Give the extent of all Plasmodium malariae-infected red blood cells.
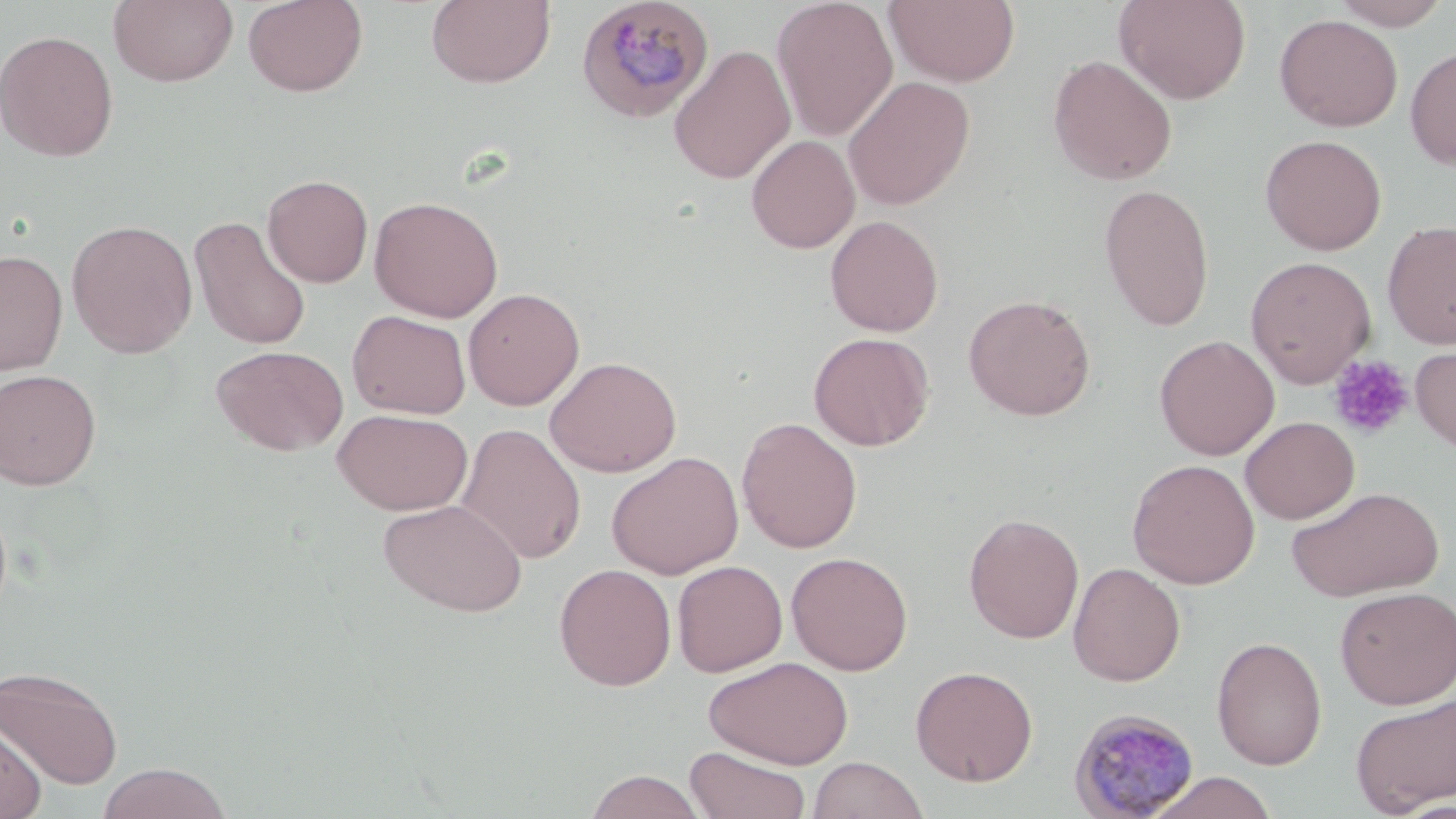

Approximate bounding boxes as named x1/y1/x2/y2 corners in pixels.
Plasmodium malariae-infected red blood cells: (x1=575, y1=0, x2=715, y2=123), (x1=1067, y1=708, x2=1201, y2=819).

Summary:
  - Platelet locations: (x1=1327, y1=354, x2=1414, y2=439)
  - Uninfected red blood cell locations: (x1=108, y1=0, x2=239, y2=87), (x1=242, y1=0, x2=368, y2=97), (x1=426, y1=0, x2=556, y2=89), (x1=772, y1=0, x2=898, y2=141), (x1=884, y1=0, x2=1021, y2=87), (x1=1114, y1=0, x2=1251, y2=104), (x1=1327, y1=0, x2=1451, y2=29), (x1=1274, y1=14, x2=1403, y2=132), (x1=0, y1=29, x2=119, y2=162), (x1=668, y1=44, x2=795, y2=184), (x1=1405, y1=45, x2=1456, y2=171), (x1=1047, y1=54, x2=1178, y2=186), (x1=842, y1=76, x2=975, y2=210), (x1=1259, y1=134, x2=1387, y2=255), (x1=747, y1=135, x2=860, y2=254), (x1=262, y1=174, x2=373, y2=287), (x1=1099, y1=184, x2=1215, y2=331), (x1=369, y1=195, x2=503, y2=322), (x1=189, y1=215, x2=312, y2=351), (x1=825, y1=215, x2=943, y2=336), (x1=66, y1=219, x2=198, y2=357), (x1=1382, y1=220, x2=1456, y2=349), (x1=0, y1=249, x2=68, y2=376), (x1=1245, y1=255, x2=1376, y2=388), (x1=463, y1=288, x2=584, y2=410), (x1=963, y1=294, x2=1096, y2=420), (x1=347, y1=309, x2=471, y2=419), (x1=808, y1=332, x2=934, y2=451), (x1=1155, y1=335, x2=1279, y2=460), (x1=1410, y1=341, x2=1456, y2=459), (x1=211, y1=344, x2=348, y2=456), (x1=544, y1=356, x2=682, y2=478), (x1=0, y1=368, x2=102, y2=490), (x1=332, y1=408, x2=472, y2=515), (x1=737, y1=416, x2=862, y2=553), (x1=1240, y1=416, x2=1359, y2=524), (x1=456, y1=423, x2=586, y2=565), (x1=606, y1=451, x2=744, y2=579), (x1=1127, y1=458, x2=1260, y2=589), (x1=1286, y1=486, x2=1444, y2=601), (x1=377, y1=498, x2=528, y2=617), (x1=964, y1=512, x2=1084, y2=643), (x1=786, y1=551, x2=913, y2=675), (x1=672, y1=560, x2=788, y2=678), (x1=1068, y1=562, x2=1185, y2=687), (x1=553, y1=563, x2=676, y2=691), (x1=1335, y1=586, x2=1456, y2=709), (x1=1211, y1=636, x2=1327, y2=770), (x1=704, y1=655, x2=853, y2=768), (x1=910, y1=665, x2=1038, y2=786), (x1=0, y1=666, x2=123, y2=787), (x1=1351, y1=694, x2=1456, y2=815), (x1=0, y1=715, x2=46, y2=819), (x1=684, y1=745, x2=811, y2=819), (x1=808, y1=757, x2=927, y2=818), (x1=96, y1=762, x2=232, y2=819), (x1=584, y1=769, x2=707, y2=819), (x1=1144, y1=771, x2=1280, y2=818)
  - Slide-level diagnosis: Plasmodium malariae
  - Modality: light microscopy
  - Magnification: 1000x
  - Preparation: thin blood film
  - Field of view: single
  - Stain: May-Grünwald-Giemsa
  - Image size: 1456×819 pixels